Point out each malaria parasite.
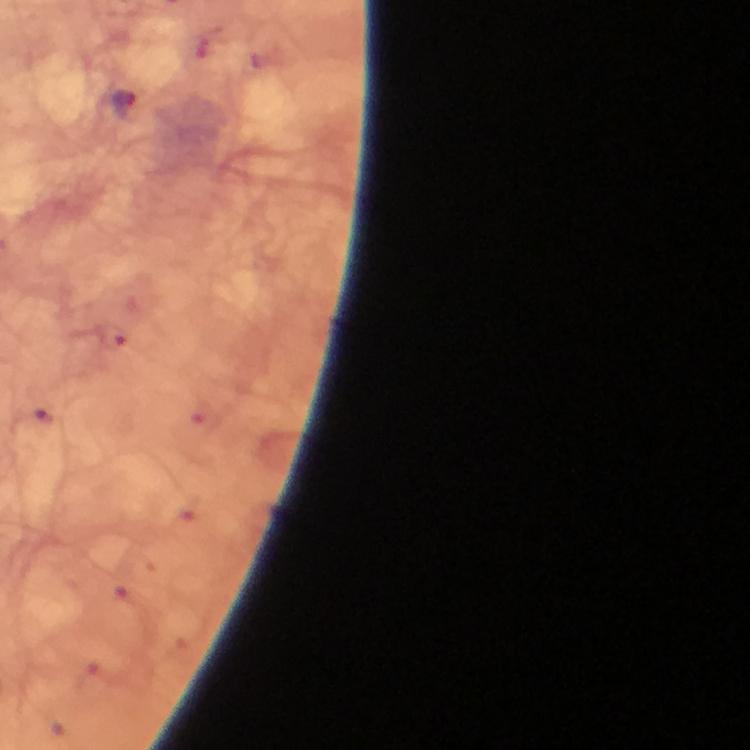

Approximate centers as (x, y) in pixels.
Malaria parasites: (125, 105), (49, 416).

immersion oil = used
context = from a malaria diagnostic workup
stain = Giemsa
image size = 750×750 pixels
capture = smartphone photograph through a microscope
preparation = thick smear
magnification = 100x
cropped from = one field of view